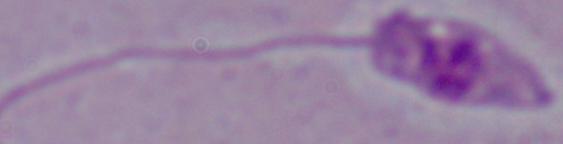
Micrograph. A Leishmania parasite is seen. 1000x magnification.